Identify the parasite.
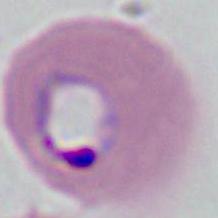
Plasmodium.

magnification = 400x or 1000x
modality = micrograph